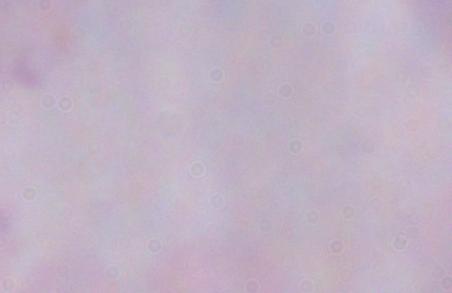
Summary:
  - Magnification: 1000x
  - Identification: trypanosome
  - Modality: photomicrograph